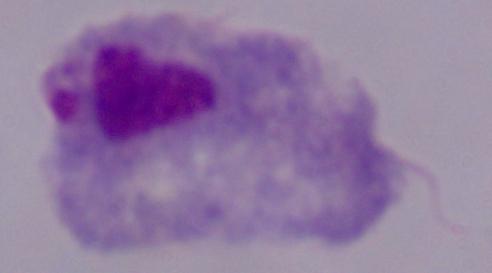 A trichomonad is seen. 1000x magnification. Micrograph.